Assess this cell for malaria.
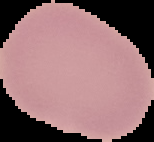

It is uninfected.

preparation = thin blood smear
image size = 154×142 pixels
image type = segmented cell region with the area outside set to black